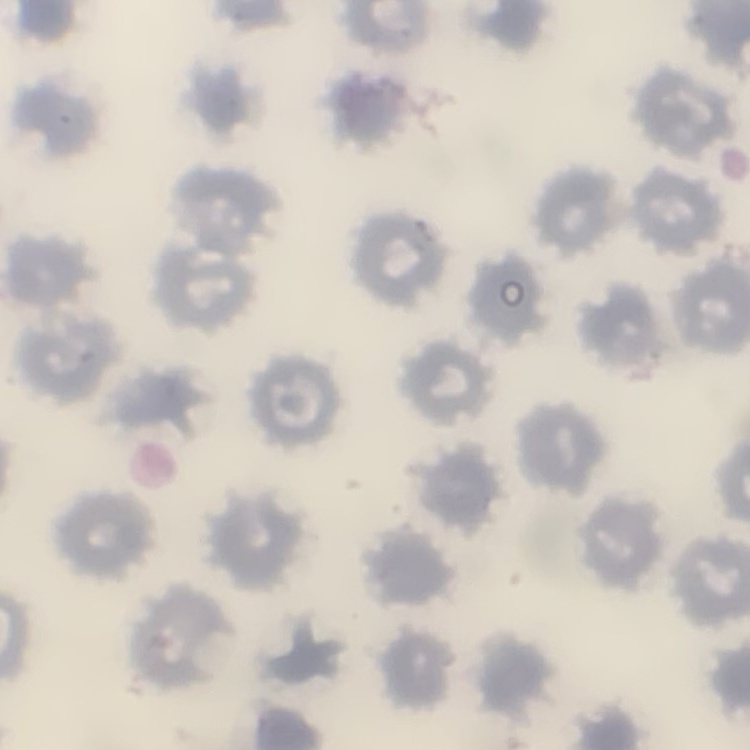
red blood cell morphology = no rouleaux formation
preparation = thin peripheral smear
image type = one tile cut from a larger photomicrograph
stain = Field's or Giemsa